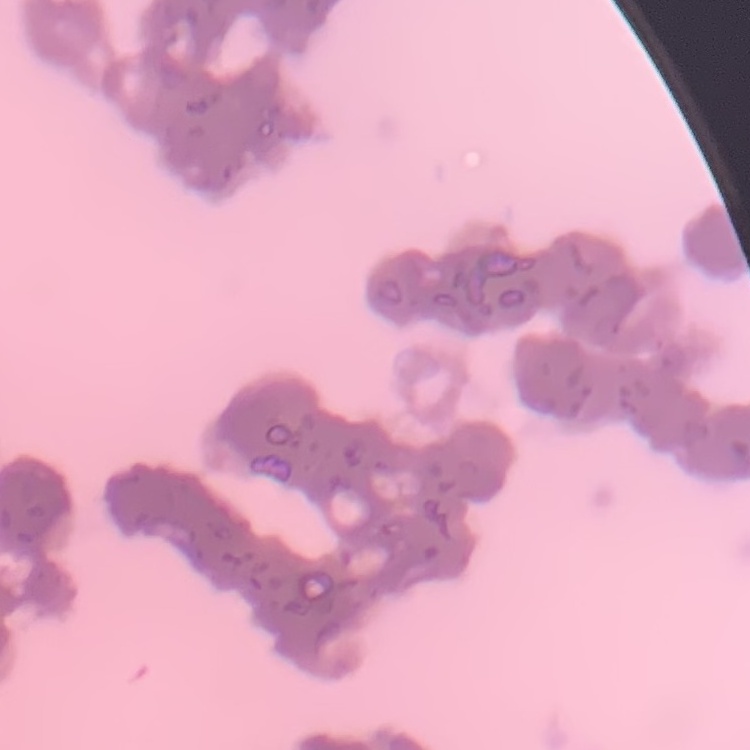

Summary:
  - Red blood cell morphology: rouleaux formation
  - Image type: one tile cut from a larger photomicrograph
  - Preparation: thin blood smear
  - Stain: Field's or Giemsa